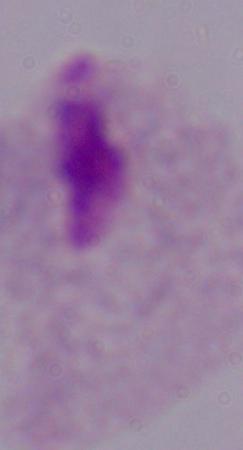

Summary:
  - Identification: trichomonad
  - Modality: micrograph
  - Magnification: 1000x